Locate every malaria parasite.
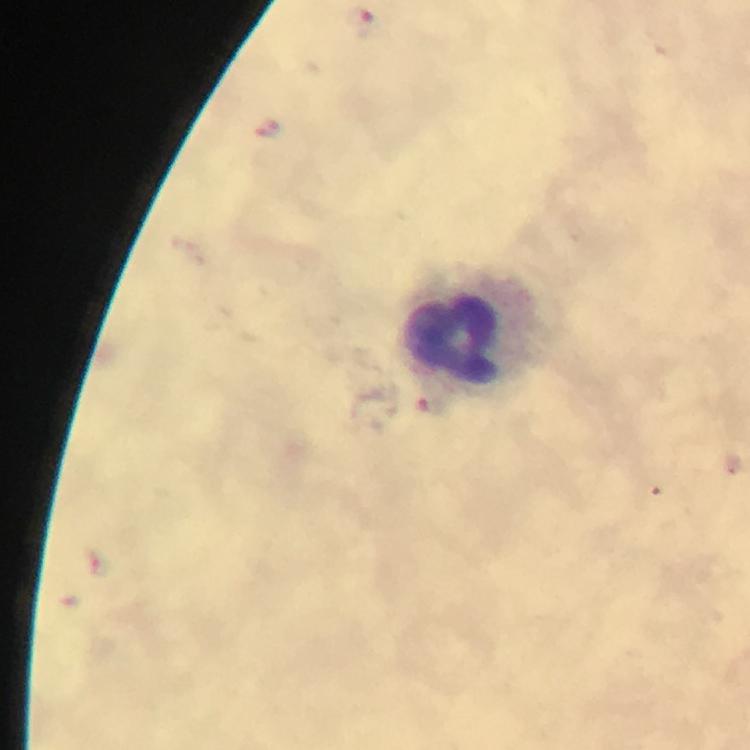

Approximate centers as [x, y] in pixels.
Malaria parasites: [360, 19], [97, 562].

{
  "magnification": "100x",
  "preparation": "thick blood film",
  "immersion_oil": "applied",
  "leukocyte_locations": "approximate centers as [x, y] in pixels: [477, 332]",
  "context": "from a malaria diagnostic workup",
  "cropped_from": "a single field of view",
  "image_size": "750×750 pixels",
  "stain": "Giemsa",
  "capture": "smartphone camera through the microscope"
}